Identify the parasite.
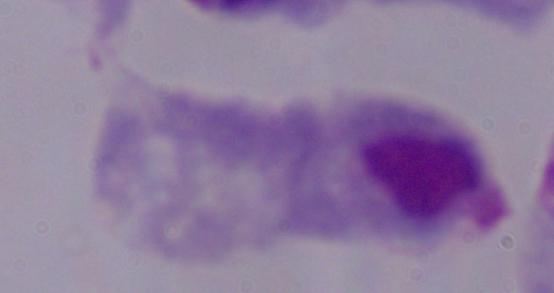
A trichomonad.

modality = micrograph
magnification = 1000x